Give the position of every malaria parasite.
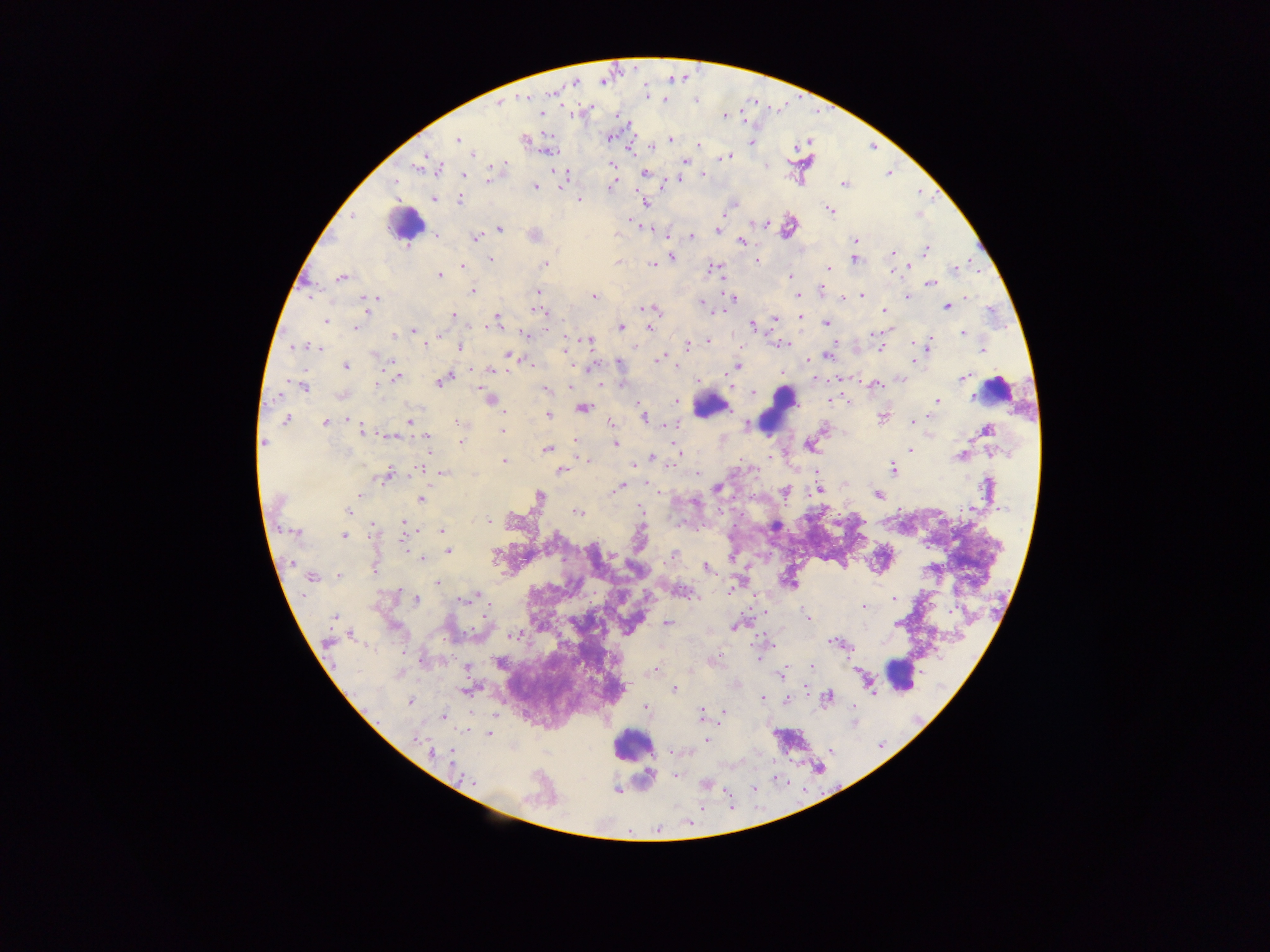
Approximate centers as x y in pixels.
Malaria parasites: 524 98; 664 100; 696 101; 499 103; 541 114; 618 116; 725 116; 610 138; 457 139; 525 140; 670 140; 751 142; 699 145; 473 154; 725 157; 685 161; 766 164; 420 166; 612 167; 495 168; 440 169; 644 172; 703 174; 464 176; 565 176; 489 178; 395 182; 665 182; 844 184; 611 186; 535 187; 435 198; 578 199; 460 201; 646 202; 733 204; 727 207; 829 210; 351 216; 630 222; 765 222; 499 229; 718 230; 436 235; 691 236; 475 238; 855 241; 741 242; 926 249; 893 252; 670 256; 490 259; 854 259; 757 261; 617 262; 545 263; 653 264; 461 267; 909 267; 828 268; 711 269; 955 269; 438 275; 790 276; 341 278; 930 283; 821 289; 472 291; 537 291; 798 295; 861 295; 594 296; 907 297; 967 297; 376 298; 733 298; 366 299; 844 299; 703 303; 947 306; 651 309; 368 310; 884 310; 539 311; 453 315; 496 317; 800 318; 774 319; 326 321; 492 322; 827 322; 752 325; 621 326; 356 327; 649 327; 413 330; 963 333; 525 334; 872 334; 393 335; 708 341; 930 341; 588 342; 425 344; 783 344; 914 344; 688 345; 459 346; 294 347; 319 348; 880 348; 983 349; 566 350; 375 355; 508 356; 827 356; 659 358; 618 363; 531 364; 345 366; 737 366; 489 370; 397 377; 446 378; 963 378; 816 380; 441 382; 377 383; 875 384; 600 385; 303 386; 546 389; 753 392; 491 400; 834 400; 938 401; 677 402; 582 408; 548 415; 882 416; 643 418; 286 420; 409 421; 913 422; 325 423; 459 423; 612 423; 668 425; 748 425; 362 430; 502 430; 986 430; 390 436; 427 437; 575 441; 460 442; 264 443; 614 444; 811 446; 548 449; 910 449; 428 450; 680 451; 960 456; 769 457; 652 458; 504 461; 588 461; 673 462; 633 466; 422 469; 893 469; 561 470; 444 474; 697 474; 386 475; 620 488; 987 488; 717 489; 615 490; 818 490; 784 492; 877 494; 361 495; 540 496; 421 499; 641 510; 349 511; 578 512; 487 522; 404 523; 372 526; 442 530; 297 532; 344 536; 403 539; 447 552; 673 555; 421 558; 291 563; 707 568; 374 569; 339 576; 311 577; 437 584; 682 592; 475 596; 894 599; 416 600; 463 600; 863 607; 334 617; 807 617; 667 623; 897 623; 737 625; 351 635; 512 635; 327 643; 836 643; 812 666; 466 667; 654 669; 780 673; 673 689; 806 689; 827 696; 762 698; 789 700; 409 701; 853 707; 646 708; 701 714; 724 714; 443 716; 488 734; 416 739; 706 740; 451 752; 431 753; 676 776; 472 782; 704 784; 616 790.

field_of_view: single
capture: mobile-phone photograph through a microscope
image_size: 1270×952 pixels
preparation: thick blood smear
country: Ghana
leukocyte_locations: 'approximate centers as x y in pixels: 406 225; 997 389; 776 405; 711 406; 899 676; 634 746'